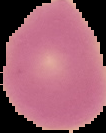

preparation = thin blood film
image type = segmented cell region with the area outside set to black
image size = 106×133 pixels
result = negative for Plasmodium parasites